Give the position of each Plasmodium falciparum parasite with its life-cycle stage, each leukocyte, and any debris.
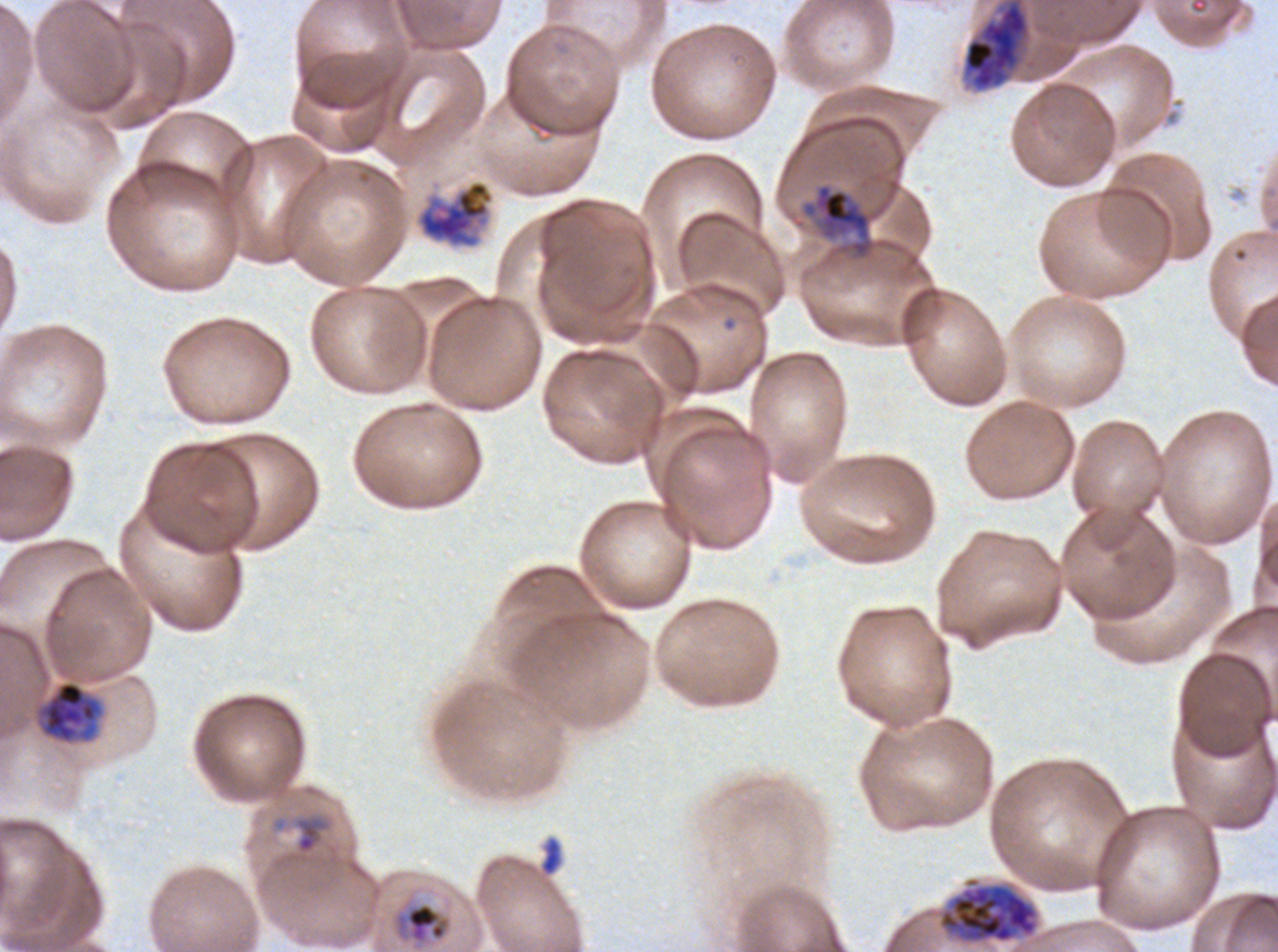
Approximate bounding boxes as [x1, y1, x2, y2] in pixels.
Rings: [295, 815, 326, 855].
Mid trophozoites: [390, 901, 453, 947].
Late trophozoites: [802, 183, 875, 259], [37, 680, 103, 744].
Early schizonts: [963, 0, 1030, 92], [416, 179, 495, 249], [938, 876, 1039, 945].
Debris: [539, 836, 563, 877].
No late-ring/early-trophozoite forms, late schizonts, segmenters, gametocytes, or leukocytes observed.

Summary:
  - Field of view: one sub-image of a larger composite
  - Life-cycle stages observed: ring, mid trophozoite, late trophozoite, early schizont
  - Specimen: Plasmodium falciparum cultured ex vivo for 24 to 48 hours, from a patient in The Gambia
  - Preparation: thin blood film
  - Image size: 1278×952 pixels
  - Stain: Giemsa